Name the blood parasite species.
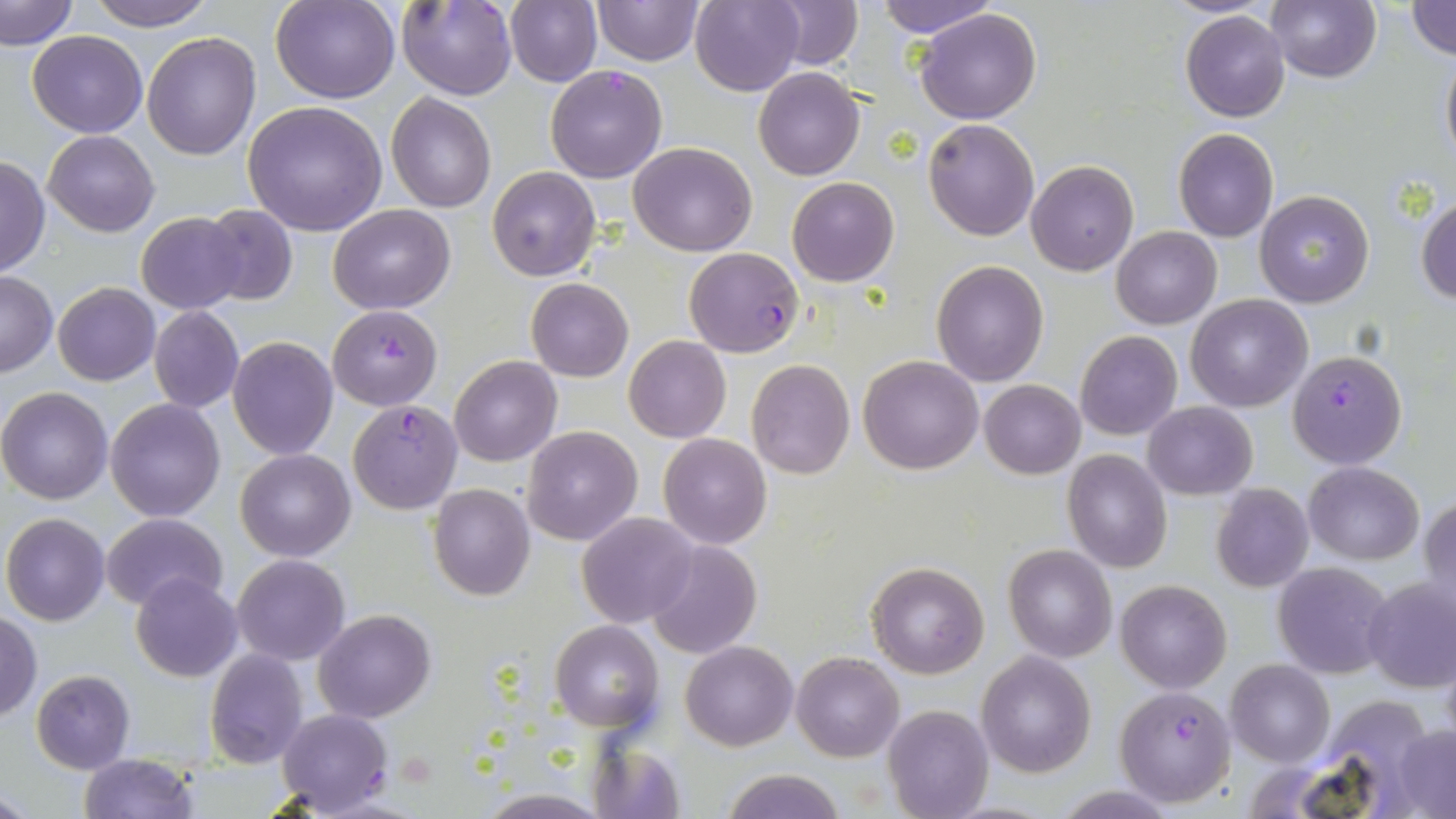

Plasmodium falciparum.

Approximate bounding boxes as [x1, y1, x2, y2] in pixels. Plasmodium falciparum-infected red blood cell locations: [396, 0, 515, 100], [545, 64, 667, 183], [685, 248, 803, 357], [328, 304, 443, 411], [1288, 350, 1407, 466], [347, 400, 462, 513], [1115, 687, 1236, 807], [276, 707, 394, 815]. Uninfected red blood cell locations: [2, 0, 78, 50], [84, 0, 221, 31], [273, 0, 399, 103], [505, 0, 602, 87], [592, 0, 704, 66], [767, 0, 862, 70], [875, 0, 1001, 38], [1265, 0, 1379, 84], [690, 1, 804, 94], [1407, 1, 1456, 62], [915, 9, 1042, 125], [1181, 10, 1290, 122], [27, 30, 147, 138], [141, 32, 262, 158], [1440, 46, 1456, 169], [754, 68, 865, 180], [386, 92, 497, 213], [242, 100, 387, 235], [922, 118, 1038, 240], [1173, 129, 1278, 242], [44, 130, 159, 236], [630, 141, 757, 256], [0, 156, 50, 278], [1026, 160, 1138, 275], [487, 166, 600, 281], [787, 176, 899, 287], [1255, 191, 1374, 309], [1415, 194, 1456, 304], [199, 204, 298, 306], [329, 204, 455, 313], [136, 212, 247, 313], [1112, 227, 1221, 328], [932, 261, 1048, 386], [0, 271, 57, 377], [525, 279, 633, 382], [53, 282, 160, 385], [1185, 294, 1312, 411], [147, 305, 244, 413], [1075, 331, 1182, 441], [228, 336, 337, 458], [624, 336, 731, 443], [449, 355, 562, 467], [858, 355, 983, 475], [747, 359, 855, 479], [979, 380, 1085, 479], [0, 387, 112, 504], [104, 398, 228, 521], [1142, 402, 1256, 499], [522, 426, 641, 545], [658, 432, 772, 549], [235, 448, 355, 561], [1062, 450, 1172, 573], [1305, 462, 1424, 564], [428, 483, 534, 600], [1210, 483, 1313, 593], [1418, 495, 1455, 618], [577, 512, 697, 628], [1, 513, 110, 626], [103, 514, 227, 612], [645, 540, 761, 659], [1003, 544, 1117, 663], [232, 554, 350, 666], [1272, 561, 1395, 679], [868, 563, 988, 678], [130, 573, 242, 682], [1362, 578, 1456, 694], [1115, 579, 1232, 694], [314, 609, 435, 723], [0, 613, 42, 722], [551, 620, 664, 734], [681, 640, 796, 750], [205, 649, 308, 768], [976, 650, 1097, 776], [792, 652, 902, 762], [1226, 659, 1334, 768], [30, 670, 136, 773], [882, 704, 993, 819], [1394, 727, 1456, 816], [589, 739, 686, 819], [78, 754, 198, 818], [720, 768, 846, 819], [0, 784, 36, 817], [1052, 785, 1181, 818], [474, 791, 612, 818]. May-Grünwald-Giemsa-stained preparation. 1000x magnification. Light microscopy. Image is 1456×819 pixels. One field of a larger specimen. Thin blood smear.